State which cell type is depicted.
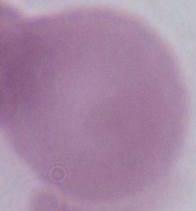
This is an erythrocyte.

modality: micrograph
magnification: 1000x